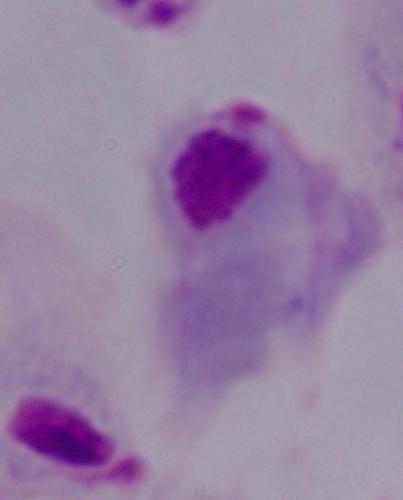
A trichomonad is shown. Captured at 1000x magnification. Micrograph.